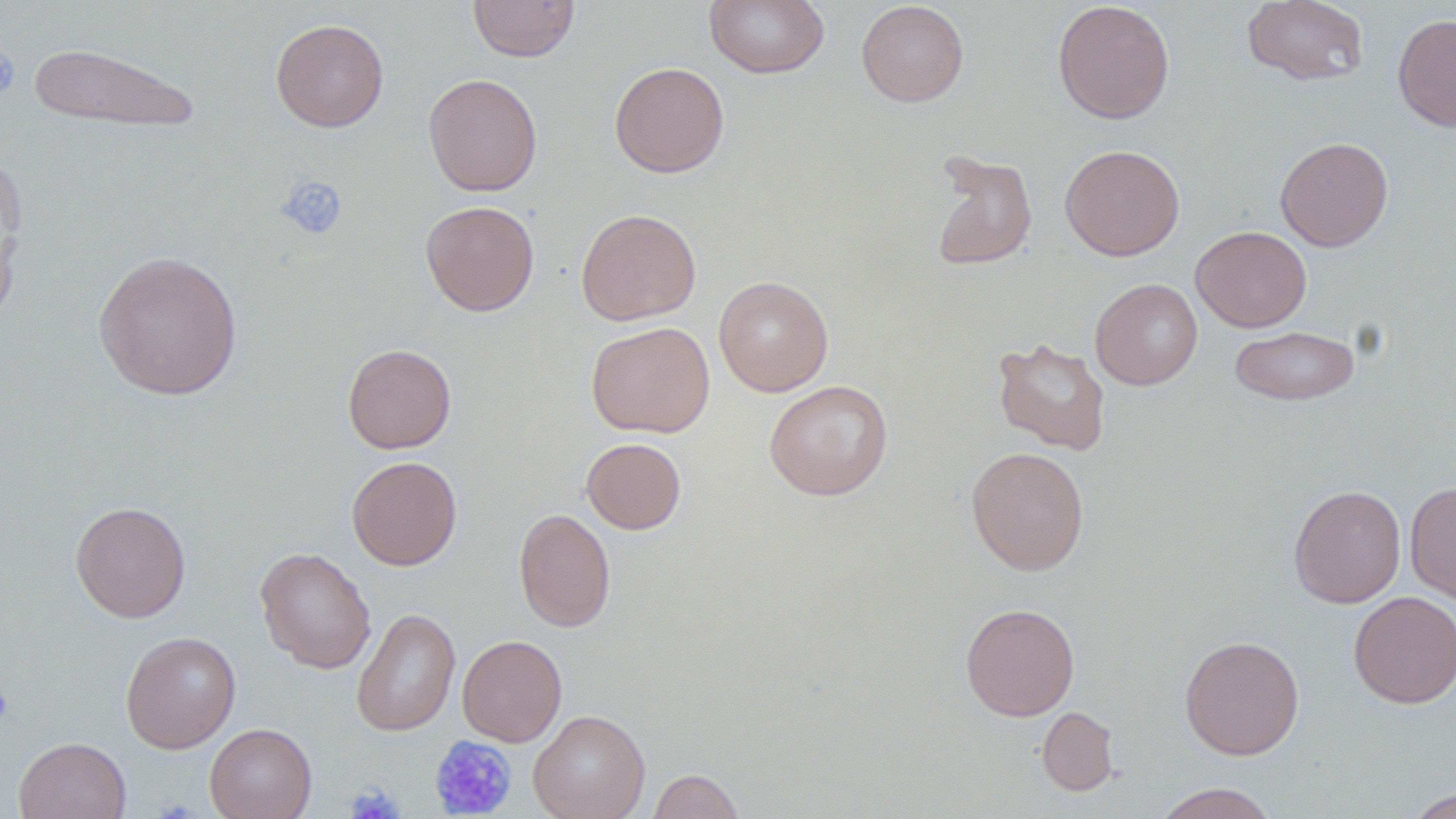
Summary:
  - Coordinate format: approximate bounding boxes as (x1, y1, x2, y2) in pixels
  - Platelet locations: (0, 47, 21, 97), (277, 175, 348, 241), (0, 681, 14, 725), (429, 735, 517, 818), (345, 783, 403, 819)
  - Uninfected red blood cell locations: (467, 0, 579, 62), (705, 0, 830, 79), (1241, 0, 1369, 86), (856, 1, 969, 107), (1052, 1, 1175, 124), (1392, 13, 1456, 132), (270, 18, 389, 132), (27, 42, 201, 135), (609, 62, 730, 178), (423, 72, 543, 197), (1275, 136, 1393, 252), (1059, 144, 1185, 261), (929, 151, 1038, 272), (0, 159, 27, 328), (420, 200, 539, 316), (576, 208, 701, 325), (1190, 225, 1312, 332), (92, 250, 244, 400), (713, 275, 834, 397), (1090, 278, 1203, 390), (586, 321, 715, 438), (1229, 325, 1360, 406), (992, 337, 1111, 455), (342, 343, 456, 453), (764, 379, 893, 500), (581, 437, 686, 534), (966, 446, 1090, 576), (347, 456, 462, 570), (1405, 481, 1456, 604), (1288, 484, 1406, 608), (70, 501, 191, 622), (514, 508, 616, 632), (254, 546, 377, 673), (1348, 591, 1456, 708), (960, 602, 1080, 721), (351, 607, 461, 737), (120, 631, 241, 753), (456, 634, 567, 747), (1179, 635, 1305, 760), (1037, 707, 1118, 796), (528, 709, 650, 819), (205, 723, 317, 819), (13, 736, 131, 818), (647, 768, 744, 819), (1151, 782, 1281, 819), (1404, 788, 1456, 818)
  - Slide-level diagnosis: no evidence of blood parasites
  - Magnification: 1000x
  - Image size: 1456×819 pixels
  - Field of view: one of a larger specimen
  - Stain: May-Grünwald-Giemsa
  - Modality: light microscopy
  - Preparation: thin blood film